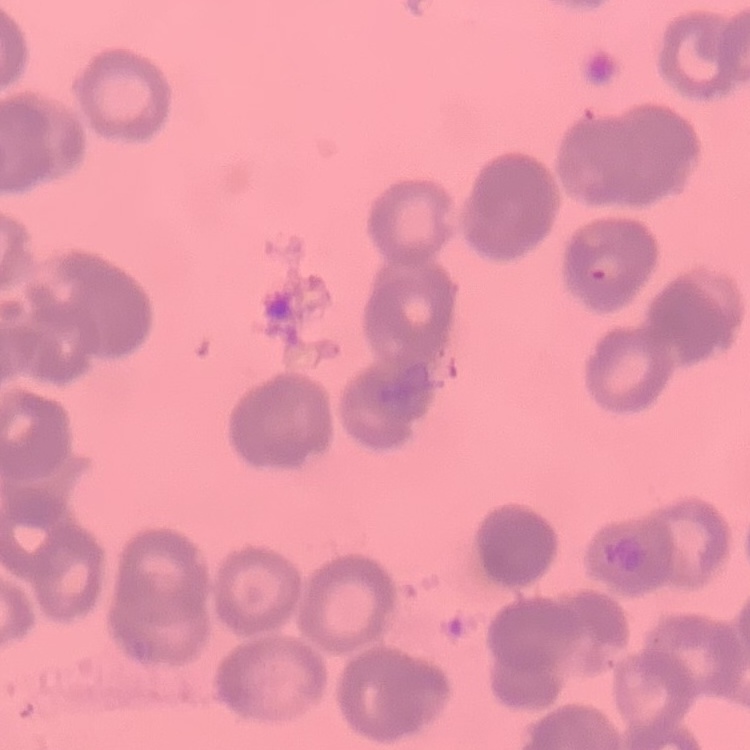

Summary:
  - Red blood cell morphology: rouleaux formation
  - Preparation: thin blood film
  - Stain: Field's or Giemsa
  - Image type: square crop of a larger photomicrograph